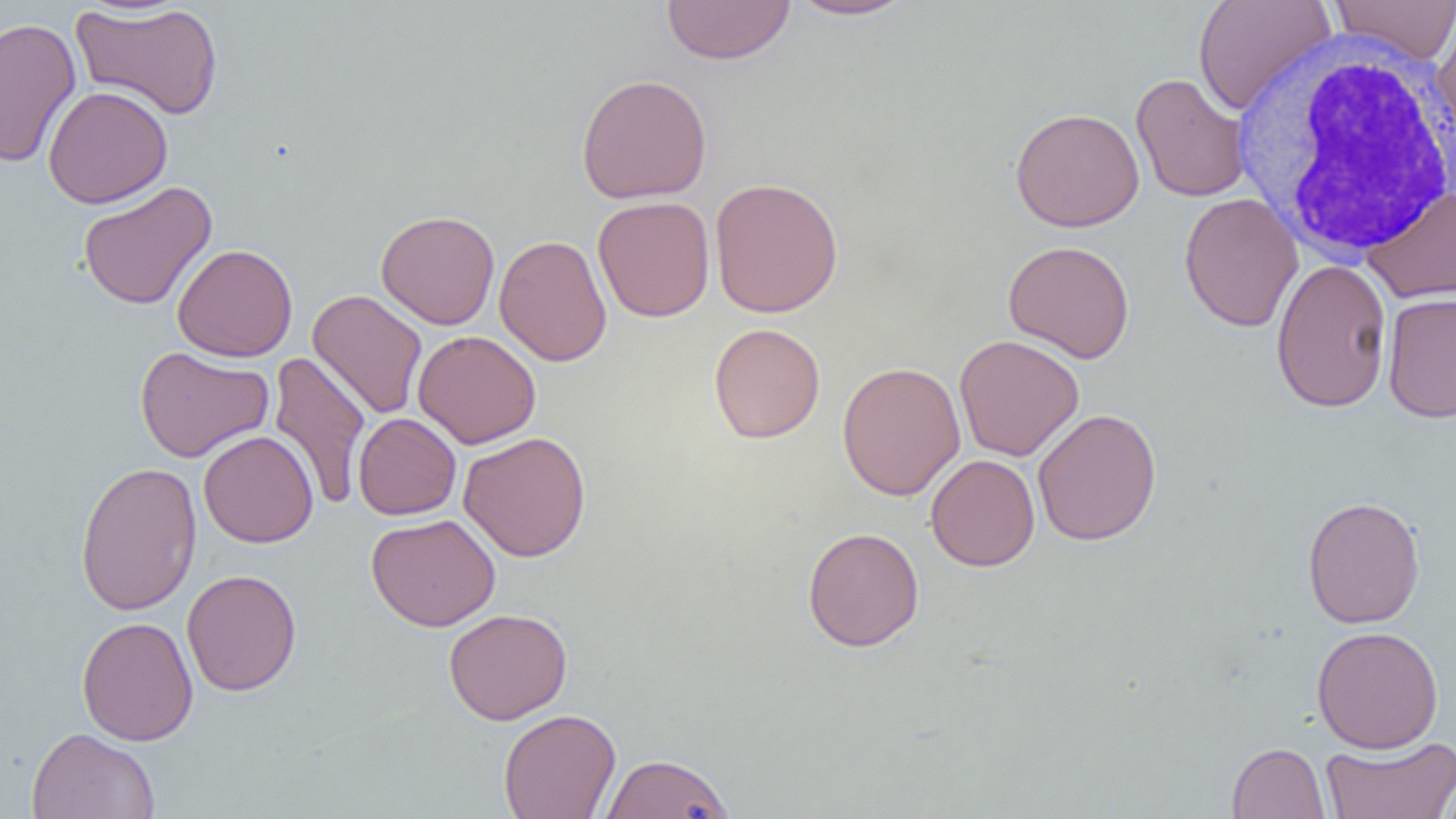

Approximate bounding boxes as (x1, y1, x2, y2) in pixels. Uninfected red blood cell locations: (661, 0, 796, 65), (786, 0, 920, 21), (1192, 0, 1336, 116), (1328, 0, 1456, 64), (71, 3, 224, 120), (1431, 8, 1456, 141), (0, 17, 82, 169), (1131, 72, 1251, 203), (575, 73, 713, 204), (43, 85, 173, 209), (1009, 107, 1145, 232), (708, 176, 844, 319), (77, 180, 217, 311), (1362, 185, 1456, 304), (1179, 193, 1303, 332), (593, 196, 715, 322), (376, 209, 500, 330), (494, 234, 612, 367), (1003, 240, 1135, 363), (172, 243, 298, 363), (1270, 259, 1393, 413), (307, 289, 428, 420), (1382, 291, 1456, 424), (709, 322, 826, 444), (412, 330, 541, 449), (954, 334, 1084, 461), (135, 345, 274, 463), (269, 351, 370, 511), (837, 361, 965, 501), (1032, 408, 1162, 546), (353, 413, 461, 520), (198, 430, 318, 548), (458, 431, 591, 562), (925, 454, 1040, 571), (74, 461, 202, 616), (1302, 495, 1425, 629), (366, 513, 501, 631), (802, 526, 925, 652), (182, 569, 302, 696), (443, 608, 573, 725), (76, 616, 198, 746), (1311, 625, 1444, 753), (498, 708, 621, 819), (26, 727, 160, 819), (1321, 735, 1456, 819), (1226, 741, 1331, 818), (599, 752, 735, 818), (1437, 771, 1456, 818). White blood cell locations: (1234, 36, 1456, 260). Slide-level diagnosis: negative for blood parasites. Image is 1456×819 pixels. Optical microscopy. Thin blood smear. Captured at 1000x magnification. Single field of view.